Assess the morphology of the erythrocytes.
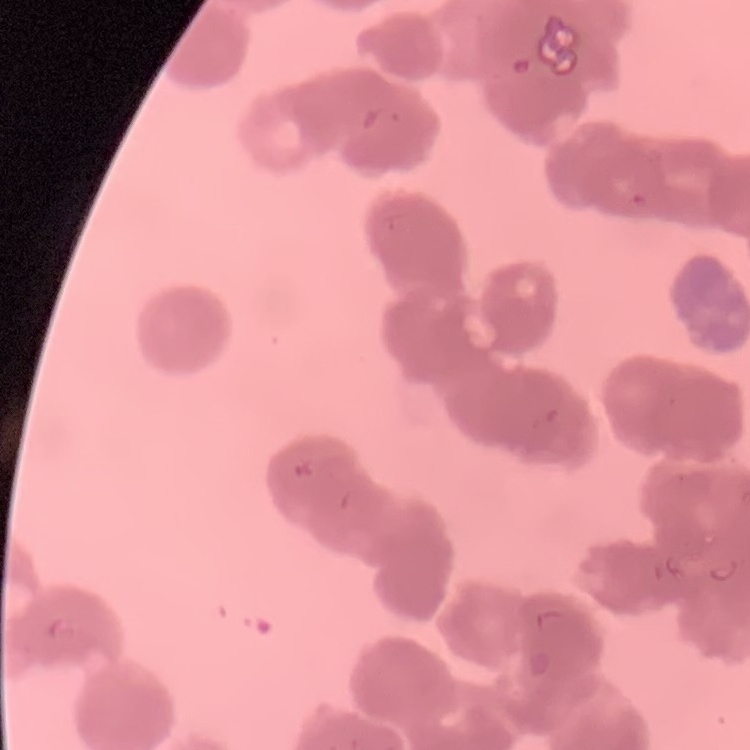
Rouleaux formation.

Thin blood film. Field's or Giemsa stain. Square crop of a larger photomicrograph.